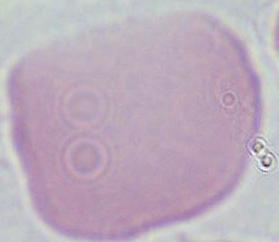
Summary:
  - Identification: red blood cell
  - Magnification: 1000x
  - Modality: photomicrograph